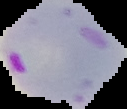
Cell region segmented out of the field of view; the surrounding area is masked to black. Image is 127×109 pixels. Malaria status: parasitized. From a thin blood film.